Classify this cell by malaria status.
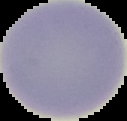
It is uninfected.

From a thin blood smear. Image is 127×121 pixels. Segmented cell region on a black background.